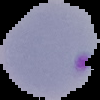
{
  "image_size": "100×100 pixels",
  "image_type": "segmented cell region with the area outside set to black",
  "preparation": "thin blood smear",
  "result": "Plasmodium parasites detected"
}